Assess this cell for malaria.
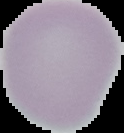

Uninfected.

image type = cell region segmented out of the field of view; surrounding area masked to black
preparation = thin blood smear
image size = 124×133 pixels